Locate every blood parasite and identify its species.
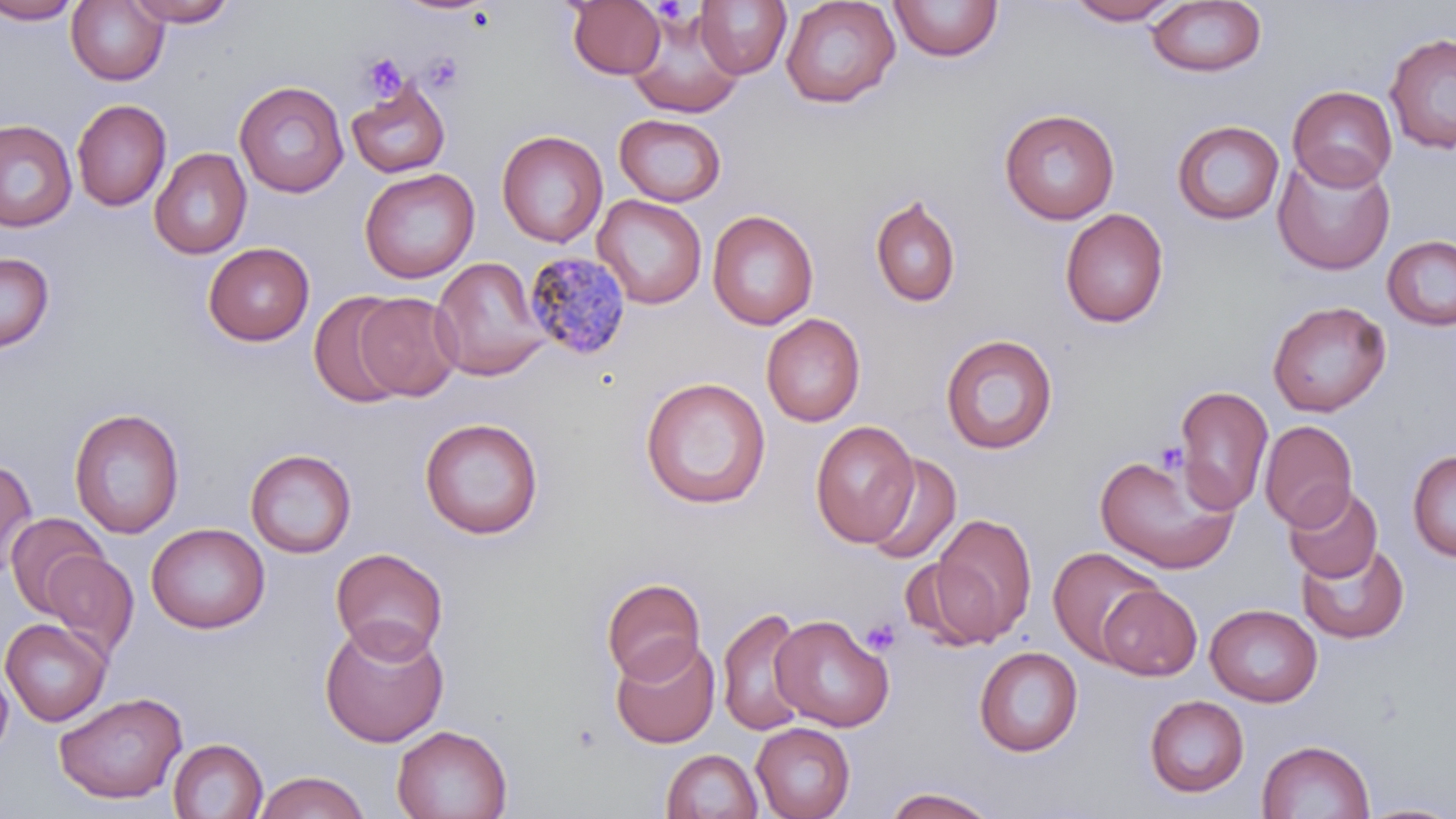

Approximate bounding boxes as named x1/y1/x2/y2 corners in pixels.
Plasmodium malariae-infected red blood cells: (x1=523, y1=251, x2=632, y2=362).
No Plasmodium falciparum, Plasmodium ovale, Plasmodium vivax, Babesia divergens, or Trypanosoma brucei observed.

Summary:
  - Platelet locations: (x1=651, y1=1, x2=690, y2=25), (x1=422, y1=52, x2=465, y2=94), (x1=360, y1=54, x2=407, y2=102), (x1=1156, y1=441, x2=1187, y2=474), (x1=860, y1=618, x2=901, y2=656)
  - Uninfected red blood cell locations: (x1=0, y1=0, x2=83, y2=24), (x1=126, y1=0, x2=238, y2=27), (x1=566, y1=0, x2=667, y2=79), (x1=694, y1=0, x2=792, y2=79), (x1=780, y1=0, x2=901, y2=109), (x1=1066, y1=0, x2=1182, y2=25), (x1=66, y1=1, x2=169, y2=85), (x1=889, y1=1, x2=1003, y2=63), (x1=1146, y1=1, x2=1267, y2=78), (x1=625, y1=9, x2=746, y2=118), (x1=1384, y1=32, x2=1456, y2=155), (x1=346, y1=78, x2=451, y2=179), (x1=234, y1=80, x2=349, y2=198), (x1=1288, y1=85, x2=1398, y2=191), (x1=72, y1=99, x2=171, y2=211), (x1=999, y1=107, x2=1120, y2=225), (x1=614, y1=114, x2=726, y2=206), (x1=0, y1=120, x2=77, y2=232), (x1=1172, y1=120, x2=1285, y2=225), (x1=496, y1=130, x2=607, y2=248), (x1=149, y1=147, x2=252, y2=259), (x1=1273, y1=152, x2=1396, y2=274), (x1=359, y1=167, x2=480, y2=284), (x1=870, y1=193, x2=962, y2=309), (x1=593, y1=194, x2=707, y2=309), (x1=1060, y1=208, x2=1169, y2=328), (x1=707, y1=209, x2=818, y2=330), (x1=1382, y1=235, x2=1456, y2=331), (x1=203, y1=242, x2=314, y2=347), (x1=0, y1=252, x2=54, y2=352), (x1=431, y1=257, x2=550, y2=381), (x1=308, y1=290, x2=410, y2=407), (x1=353, y1=293, x2=462, y2=401), (x1=1267, y1=300, x2=1391, y2=417), (x1=761, y1=313, x2=866, y2=426), (x1=940, y1=332, x2=1058, y2=454), (x1=639, y1=377, x2=771, y2=509), (x1=1173, y1=385, x2=1274, y2=514), (x1=69, y1=407, x2=185, y2=540), (x1=419, y1=417, x2=543, y2=539), (x1=810, y1=420, x2=919, y2=547), (x1=1259, y1=420, x2=1358, y2=531), (x1=245, y1=448, x2=357, y2=559), (x1=1091, y1=448, x2=1240, y2=575), (x1=1407, y1=450, x2=1456, y2=561), (x1=863, y1=452, x2=962, y2=565), (x1=0, y1=458, x2=38, y2=577), (x1=1283, y1=483, x2=1383, y2=583), (x1=5, y1=512, x2=107, y2=616), (x1=930, y1=513, x2=1038, y2=644), (x1=146, y1=522, x2=270, y2=634), (x1=1295, y1=541, x2=1410, y2=643), (x1=1048, y1=545, x2=1163, y2=664), (x1=330, y1=547, x2=449, y2=661), (x1=42, y1=549, x2=139, y2=659), (x1=601, y1=578, x2=706, y2=684), (x1=1097, y1=583, x2=1202, y2=680), (x1=1204, y1=603, x2=1322, y2=707), (x1=716, y1=607, x2=811, y2=738), (x1=770, y1=615, x2=894, y2=732), (x1=0, y1=618, x2=111, y2=726), (x1=319, y1=619, x2=449, y2=747), (x1=610, y1=637, x2=720, y2=749), (x1=974, y1=646, x2=1083, y2=756), (x1=0, y1=663, x2=14, y2=757), (x1=54, y1=692, x2=187, y2=804), (x1=1144, y1=695, x2=1249, y2=797), (x1=751, y1=723, x2=856, y2=819), (x1=392, y1=725, x2=512, y2=819), (x1=168, y1=738, x2=268, y2=819), (x1=1256, y1=738, x2=1375, y2=819), (x1=662, y1=748, x2=762, y2=819), (x1=254, y1=771, x2=369, y2=819), (x1=881, y1=787, x2=999, y2=818), (x1=1358, y1=801, x2=1456, y2=818)
  - Slide-level diagnosis: Plasmodium malariae
  - Image size: 1456×819 pixels
  - Modality: optical microscopy
  - Stain: May-Grünwald-Giemsa
  - Magnification: 1000x
  - Preparation: thin blood film
  - Field of view: single